Look for parasitized red blood cells.
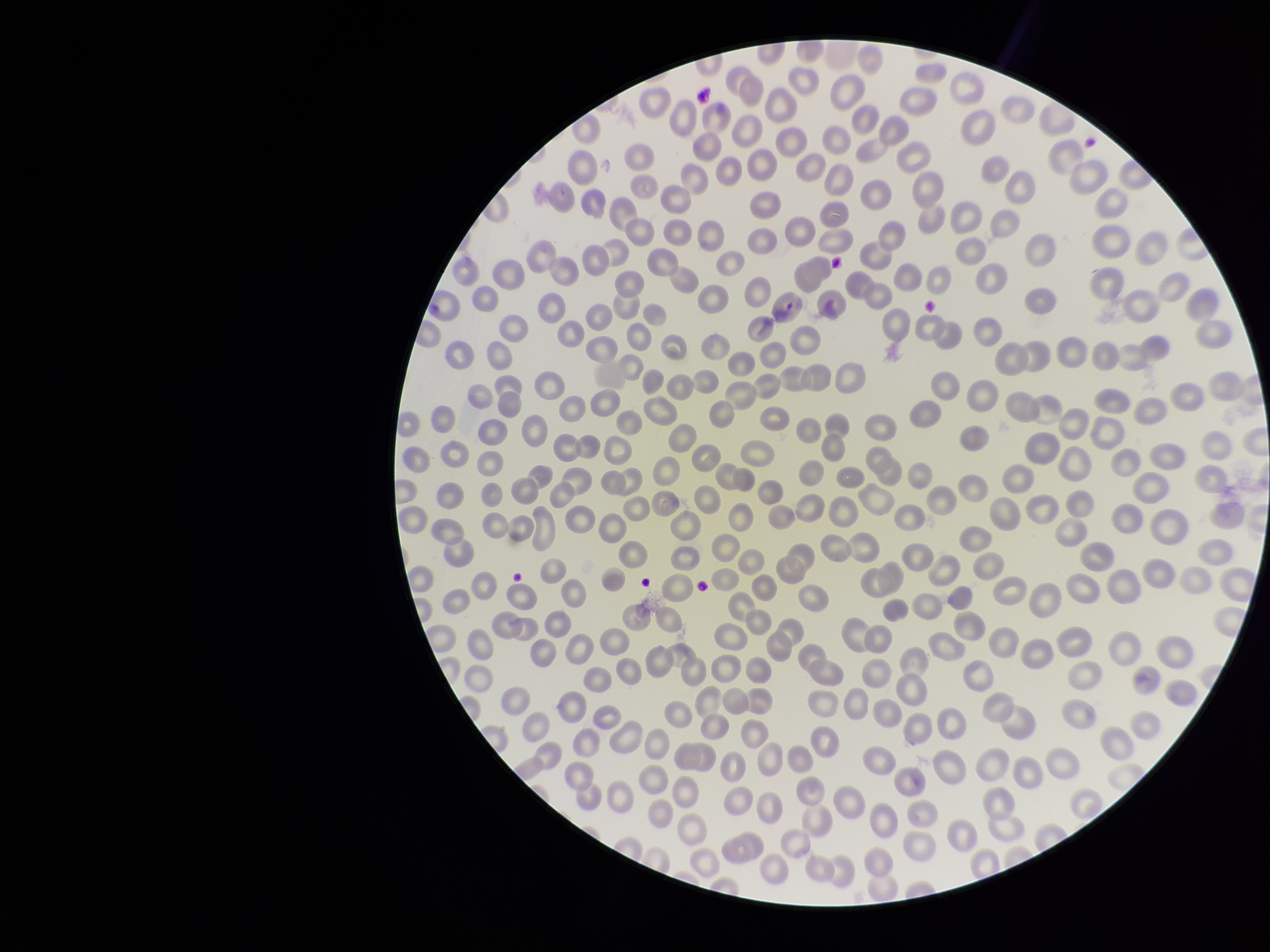
Detected.

field of view = one from this slide
species reported for this patient = Plasmodium vivax
parasitized red blood cell count = 1
patient malaria status = positive
red blood cell count = 308
image size = 1270×952 pixels
stain = Giemsa
preparation = thin blood smear
capture = smartphone photograph through the microscope eyepiece